State which cell type is depicted.
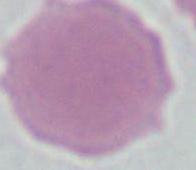
An erythrocyte.

Summary:
  - Modality: photomicrograph
  - Magnification: 1000x